Locate every blood parasite and identify its species.
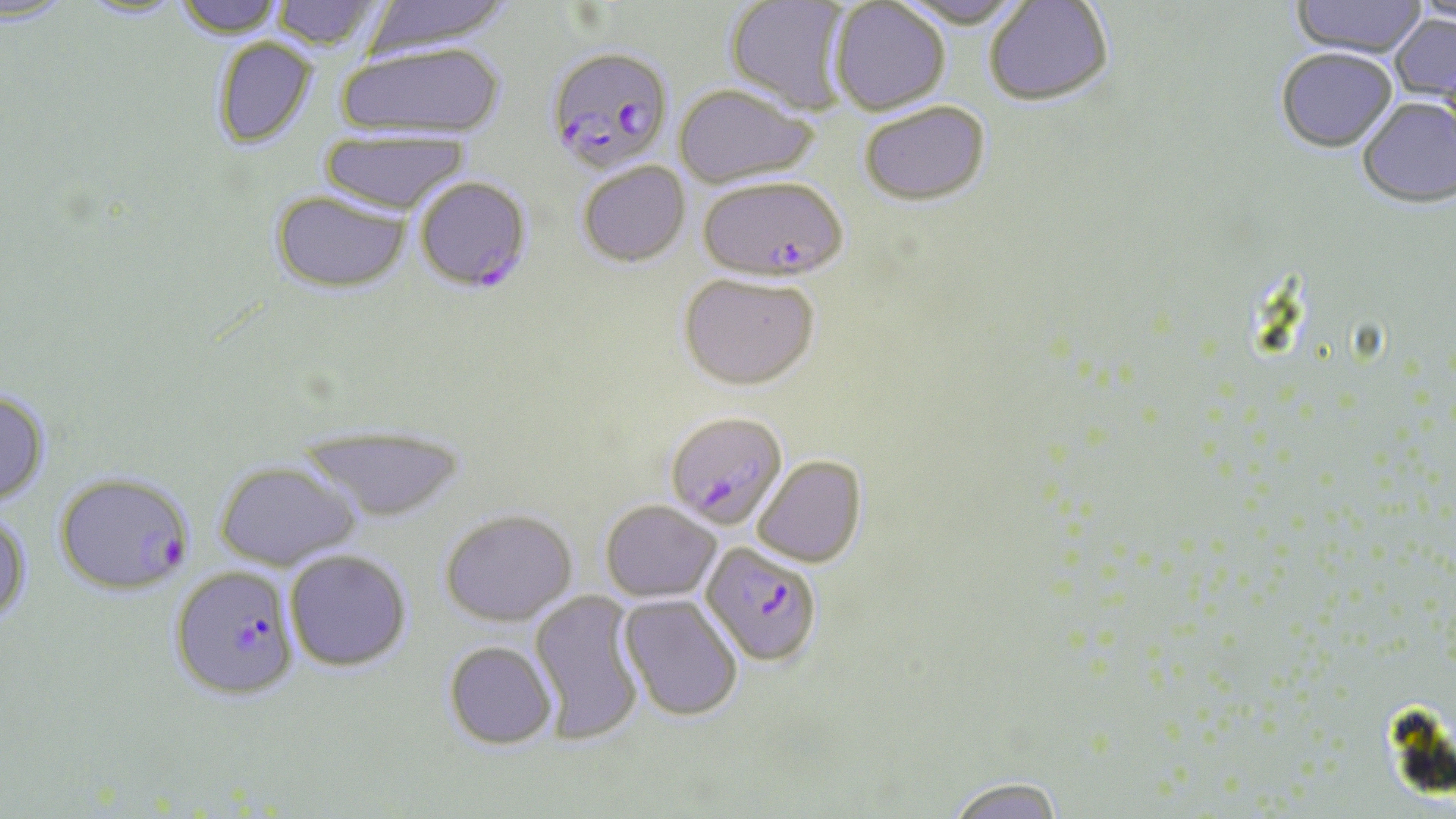
Approximate bounding boxes as [x1, y1, x2, y2] in pixels.
Plasmodium falciparum-infected red blood cells: [545, 46, 674, 174], [415, 176, 533, 292], [698, 176, 849, 282], [670, 415, 788, 529], [54, 472, 194, 596], [701, 543, 823, 666], [168, 567, 298, 700].
No Plasmodium ovale, Plasmodium malariae, Plasmodium vivax, Babesia divergens, or Trypanosoma brucei observed.

Summary:
  - Uninfected red blood cell locations: [0, 0, 77, 28], [173, 0, 287, 39], [270, 0, 386, 51], [362, 0, 513, 56], [725, 0, 853, 116], [895, 0, 1028, 30], [1289, 0, 1427, 61], [76, 1, 190, 22], [985, 1, 1113, 108], [829, 2, 951, 116], [1390, 14, 1456, 109], [210, 38, 318, 148], [337, 42, 505, 139], [1275, 51, 1397, 156], [673, 85, 818, 189], [1357, 100, 1456, 212], [859, 102, 990, 206], [320, 131, 469, 214], [578, 162, 691, 266], [271, 190, 412, 293], [678, 273, 820, 390], [0, 389, 51, 508], [298, 427, 468, 523], [753, 455, 866, 567], [214, 461, 361, 571], [600, 499, 722, 601], [440, 509, 577, 626], [0, 512, 32, 627], [285, 549, 411, 671], [530, 590, 645, 745], [619, 596, 744, 721], [443, 641, 557, 750], [944, 776, 1065, 819]
  - Slide-level diagnosis: Plasmodium falciparum
  - Image size: 1456×819 pixels
  - Stain: May-Grünwald-Giemsa
  - Preparation: thin blood smear
  - Magnification: 1000x
  - Field of view: single
  - Modality: light microscopy